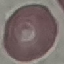 Result: no malaria parasites seen. Giemsa stain. Thin blood film. Automatically extracted cell patch, resized to 64 × 64 pixels. Photographed with a smartphone camera at the microscope eyepiece.